Classify this cell by malaria status.
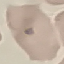

Uninfected.

{
  "stain": "Giemsa",
  "capture": "smartphone through the microscope eyepiece",
  "image_type": "automatically extracted cell patch, resized to 64 × 64 pixels",
  "preparation": "thin blood smear"
}